Assess this cell for malaria.
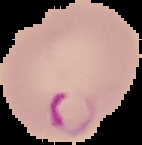

It is parasitized.

{
  "preparation": "thin blood film",
  "image_size": "142×145 pixels",
  "image_type": "segmented cell region with the area outside set to black"
}